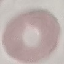
Summary:
  - Malaria status: uninfected
  - Preparation: thin smear
  - Capture: smartphone camera at the microscope eyepiece
  - Image type: cell patch, automatically extracted from a larger field of view and resized to 64 × 64 pixels
  - Stain: Giemsa